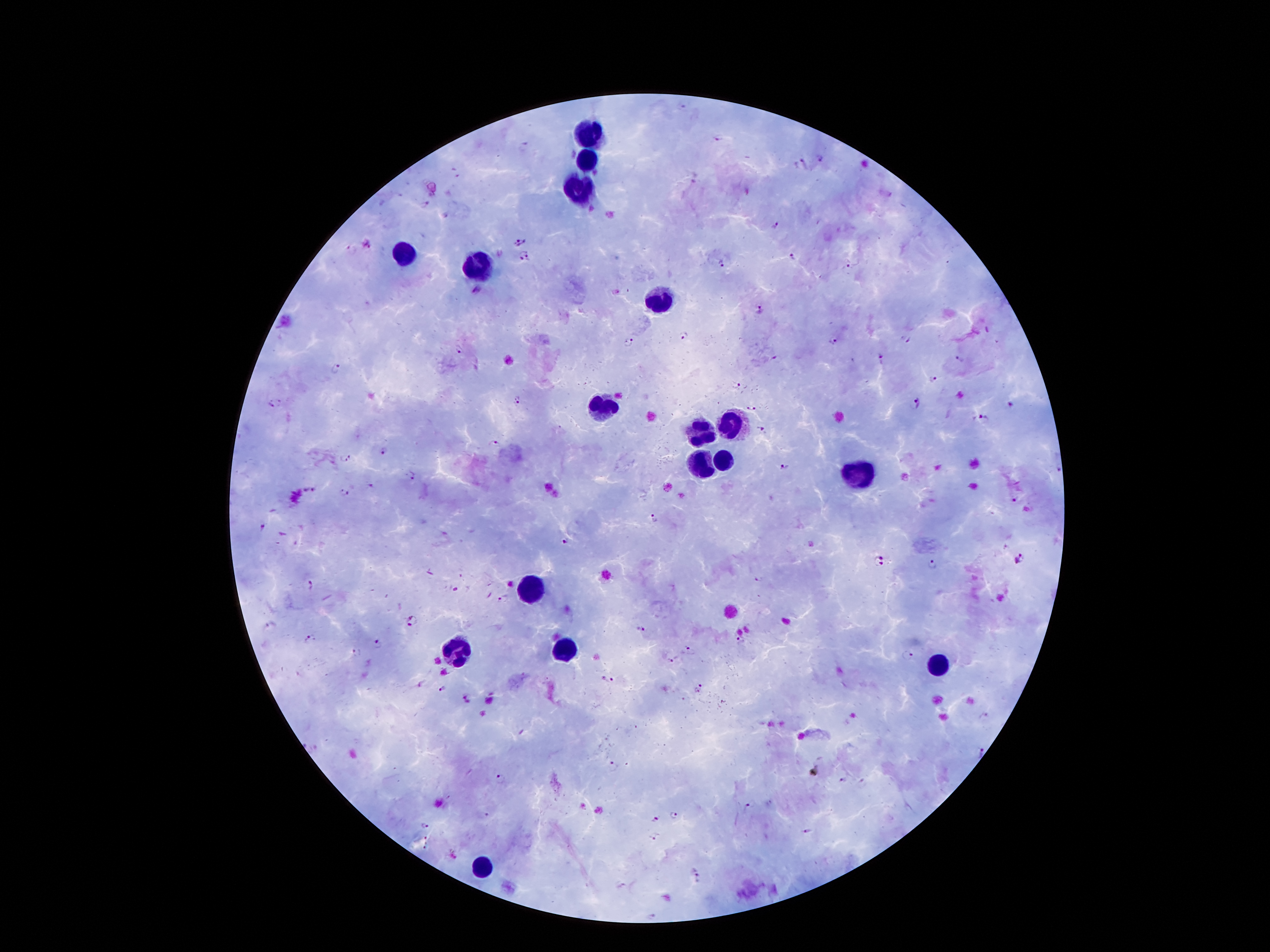 Approximate centers as [x, y] in pixels. Leukocyte locations: [588, 132], [586, 161], [580, 189], [401, 253], [475, 271], [660, 302], [606, 406], [735, 423], [701, 433], [699, 460], [727, 460], [862, 472], [533, 587], [455, 650], [567, 650], [940, 663], [487, 864]. Plasmodium parasite locations: [719, 137], [821, 158], [799, 161], [424, 204], [776, 227], [520, 242], [368, 244], [352, 249], [525, 251], [791, 256], [524, 262], [722, 263], [848, 270], [477, 290], [760, 310], [685, 335], [834, 341], [908, 341], [628, 344], [459, 350], [879, 356], [778, 358], [959, 360], [337, 368], [934, 379], [738, 386], [517, 400], [917, 402], [270, 404], [1011, 405], [751, 408], [984, 419], [763, 429], [494, 444], [383, 449], [345, 457], [784, 468], [1059, 468], [411, 474], [370, 485], [307, 491], [343, 491], [1015, 501], [653, 519], [263, 527], [564, 541], [1019, 559], [879, 562], [932, 566], [310, 585], [504, 598], [412, 620], [270, 626], [642, 630], [310, 637], [739, 640], [380, 645], [691, 652], [356, 653], [908, 656], [672, 660], [606, 680], [442, 689], [700, 690], [466, 698], [984, 716], [980, 753], [613, 766], [502, 780], [841, 780], [863, 783], [449, 799], [752, 804], [674, 815], [657, 818], [426, 826], [809, 832], [429, 837], [654, 838], [427, 850], [695, 870], [652, 915]. Single field of view. Thick peripheral-blood smear. Patient malaria status: infected with Plasmodium falciparum. Image is 1270×952 pixels. Smartphone photograph taken through the microscope eyepiece. Giemsa-stained preparation. 100x magnification.